Describe the morphology of the red blood cells.
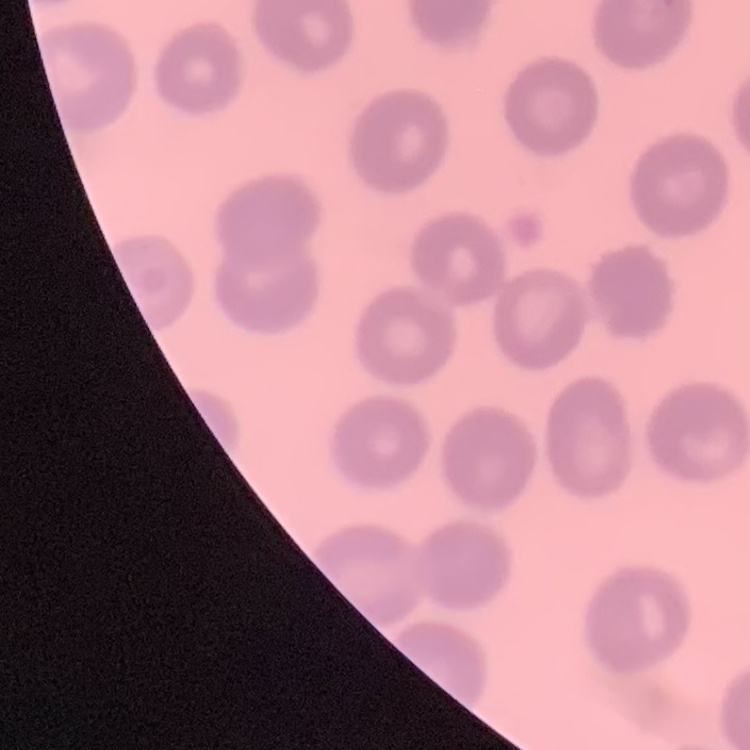

No rouleaux formation.

Field's or Giemsa stain. One tile cut from a larger photomicrograph. Thin blood smear.